Classify this cell by malaria status.
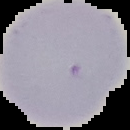
It is uninfected.

Image is 130×130 pixels. Cell region segmented out of the field of view; the surrounding area is masked to black. From a thin blood film.